Give the position of every Plasmodium falciparum parasite, noting its life-cycle stage.
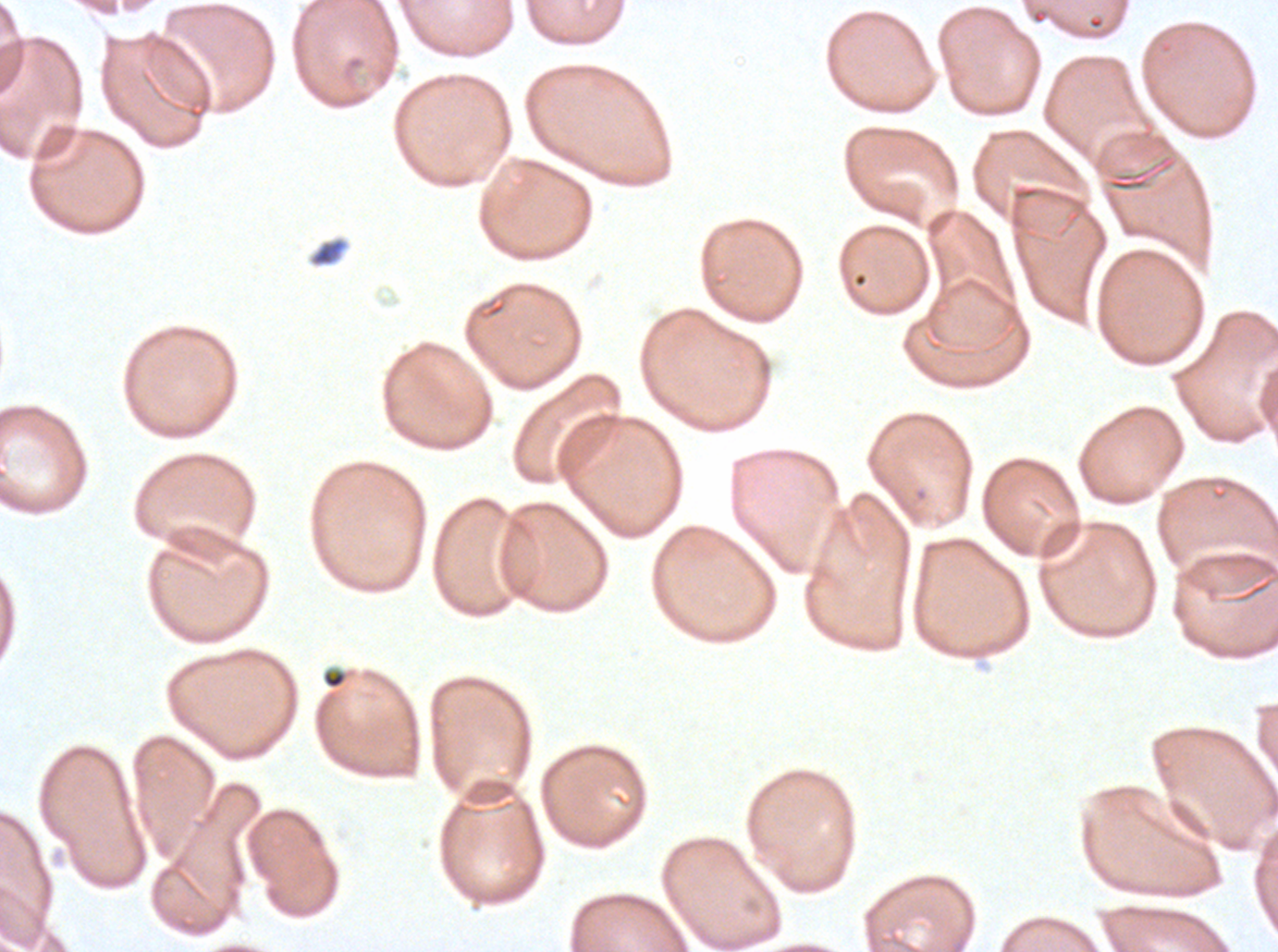
No rings, late-ring/early-trophozoite forms, mid trophozoites, late trophozoites, early schizonts, late schizonts, segmenters, or gametocytes observed.

Approximate bounding boxes as (x1, y1, x2, y2) in pixels. Debris locations: (309, 237, 348, 267), (321, 667, 349, 690). Thin blood smear. One sub-image of a larger composite. Image is 1278×952 pixels. Giemsa stain. Plasmodium falciparum from a patient in The Gambia, cultured ex vivo for 24 to 48 hours.